Comment on the morphology of the erythrocytes.
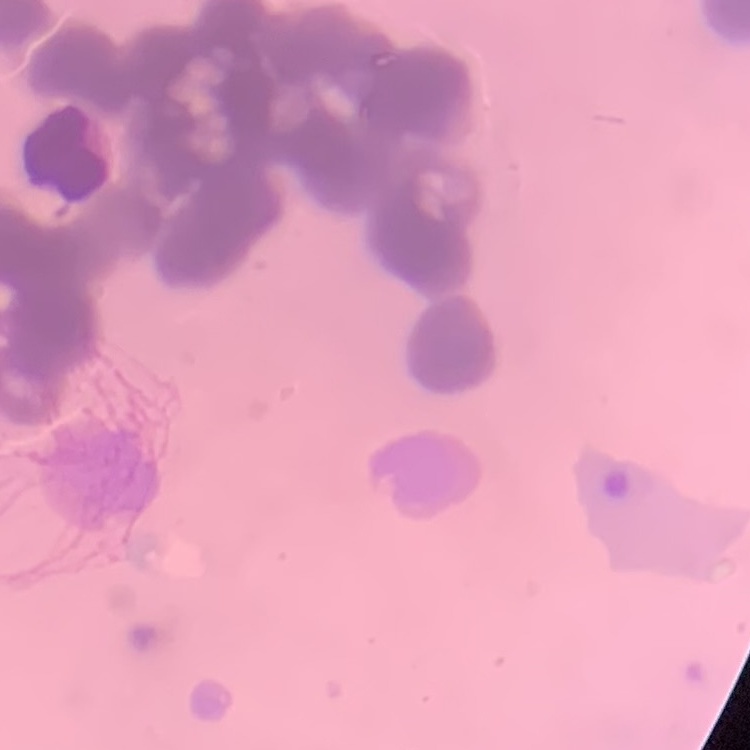

Rouleaux formation.

stain = Field's or Giemsa
image type = square crop of a larger photomicrograph
preparation = thin blood smear